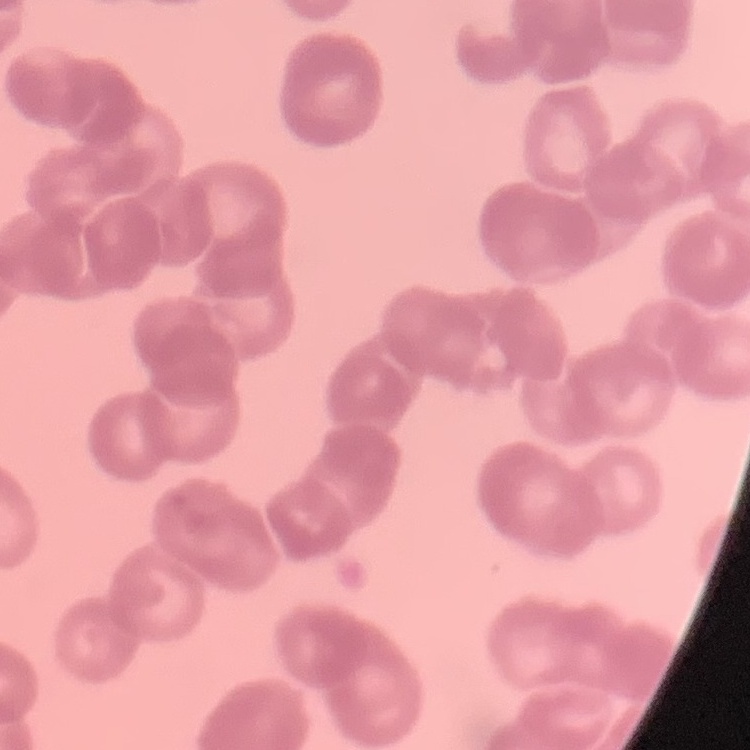 The red blood cells show rouleaux formation. Thin blood film. Field's or Giemsa stain. One tile cut from a larger photomicrograph.